State which parasite is depicted.
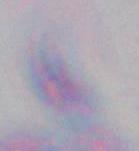

Toxoplasma gondii.

modality = micrograph
magnification = 1000x